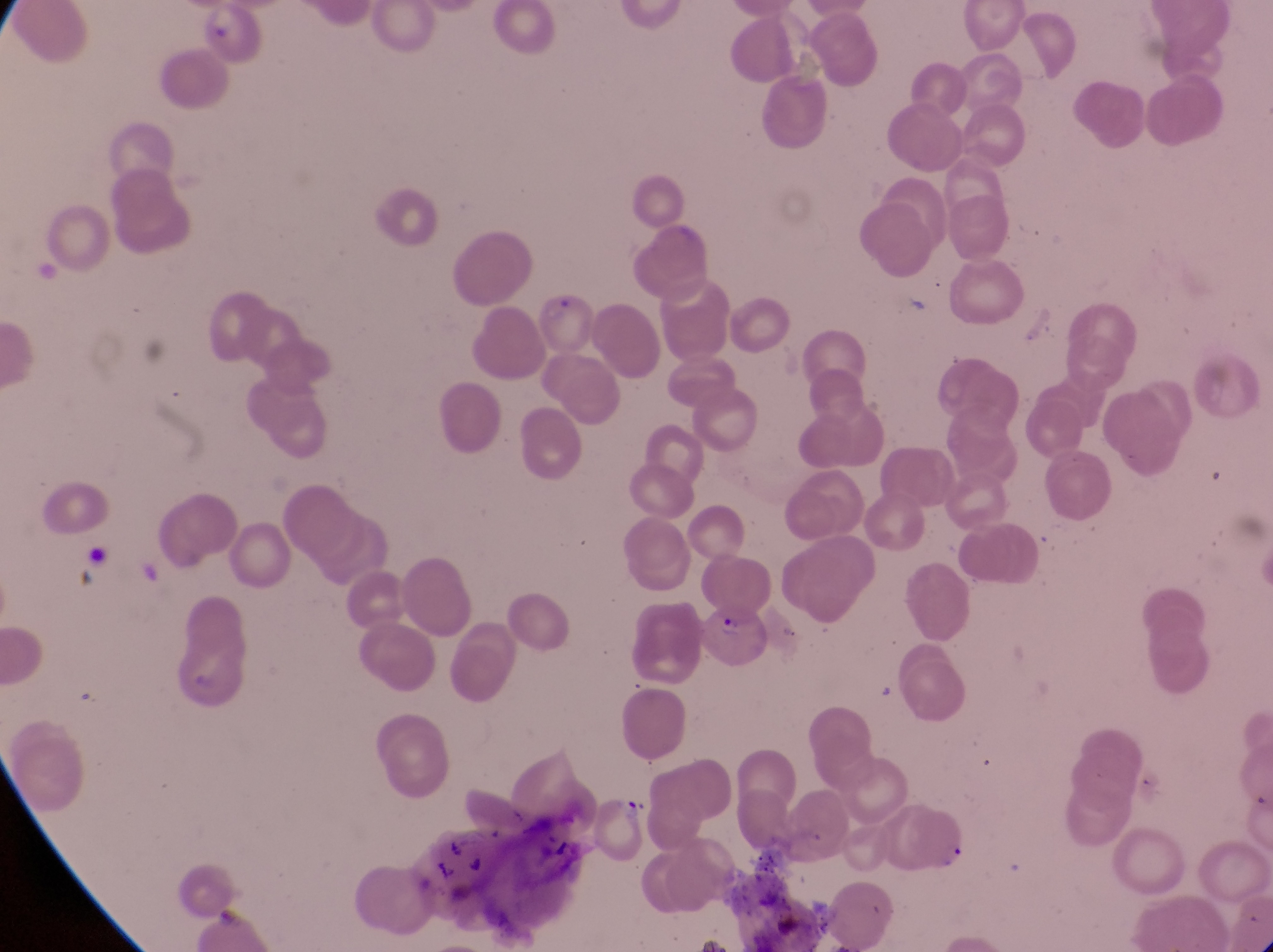
Approximate bounding boxes as (left, top, right, bottom) in pixels.
Summary:
  - Artifact (platelet-like body, stain precipitate, or debris) locations: (617, 794, 652, 827)
  - Parasitised red blood cell locations: (535, 290, 604, 364), (701, 599, 773, 674)
  - Capture: smartphone photograph through the eyepiece of an Olympus CX-23 microscope
  - Preparation: thin blood film
  - Image size: 1273×952 pixels
  - Field of view: single
  - Magnification: 1000x
  - Country: Uganda